State which parasite is depicted.
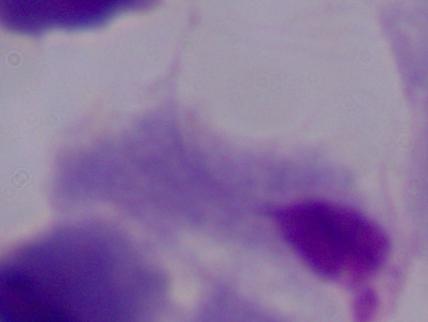

A trichomonad.

{
  "modality": "micrograph",
  "magnification": "1000x"
}